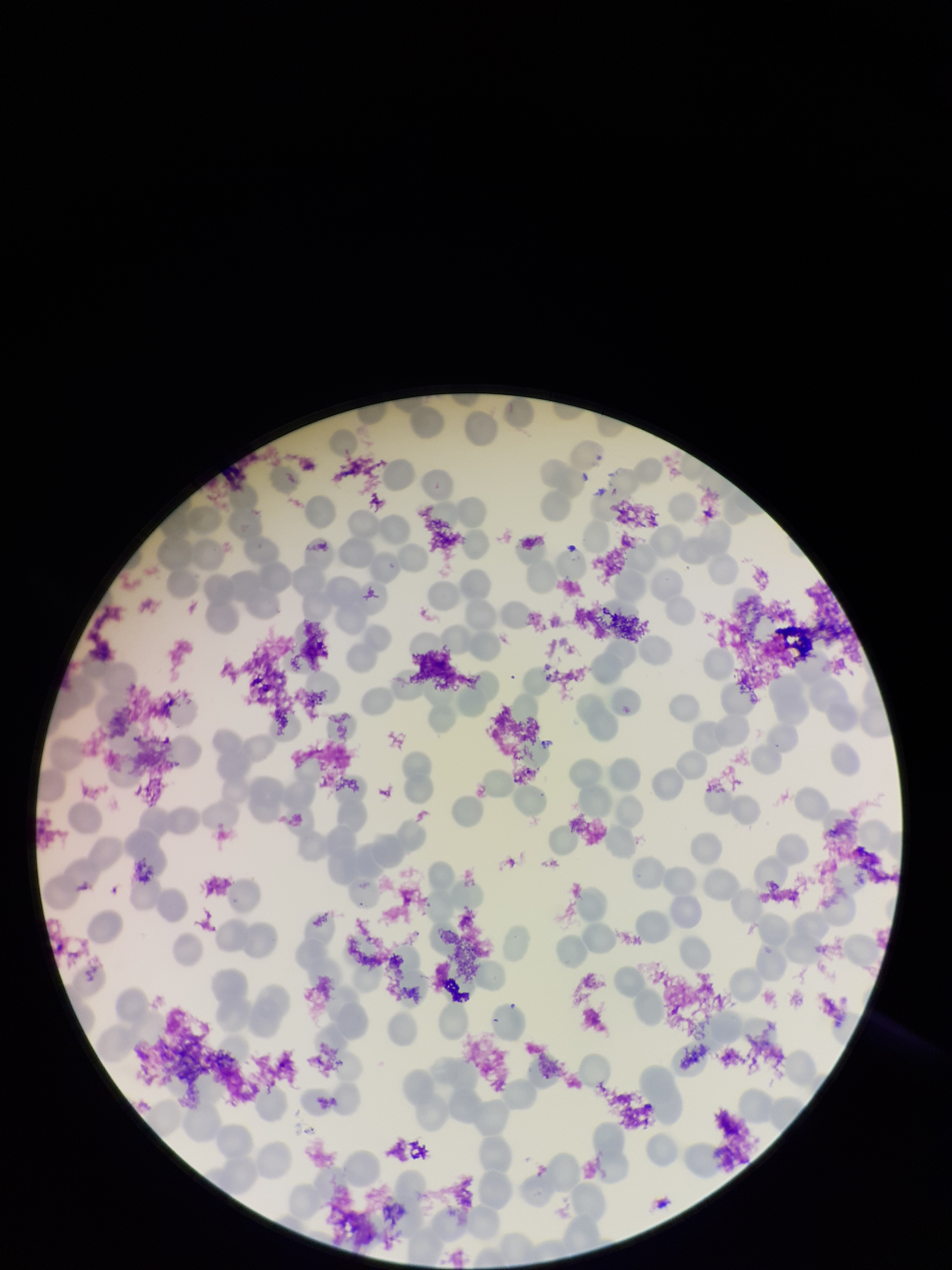

Preparation: thin. Patient malaria status: positive. Species reported for this patient: Plasmodium falciparum. Photographed through the microscope eyepiece with a smartphone camera. Parasitized red blood cells: none identified. Red blood cell count: 199. Stained with Giemsa. Image is 952×1270 pixels. Parasitized red blood cell count: 0. One field from this slide.